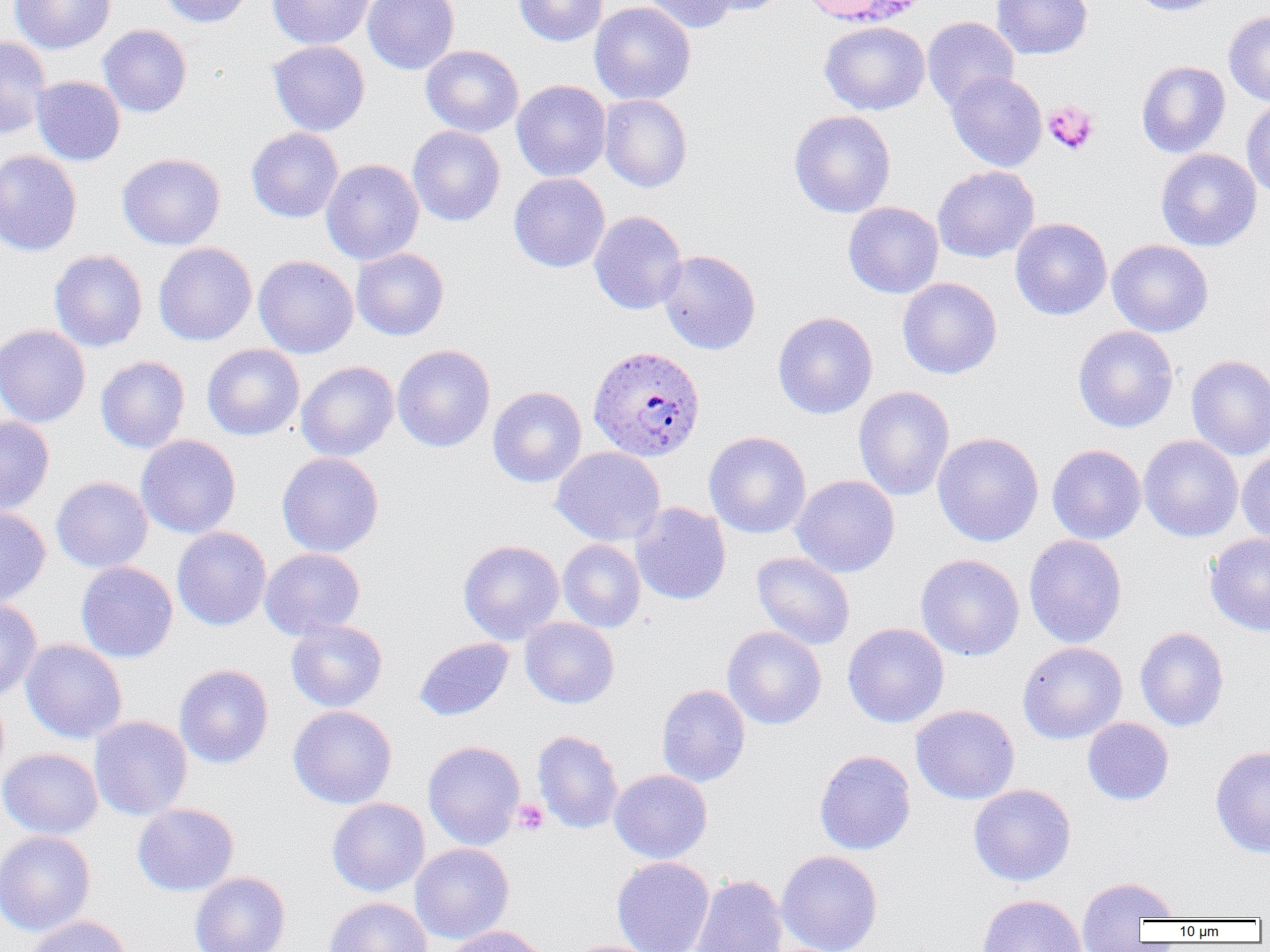
{
  "slide_level_diagnosis": "Plasmodium ovale",
  "image_size": "1270×952 pixels",
  "platelet_locations": "approximate bounding boxes as named x1/y1/x2/y2 corners in pixels: (x1=1042, y1=101, x2=1099, y2=155), (x1=511, y1=799, x2=549, y2=837)",
  "plasmodium_ovale_infected_red_blood_cell_locations": "approximate bounding boxes as named x1/y1/x2/y2 corners in pixels: (x1=588, y1=345, x2=705, y2=462)",
  "uninfected_red_blood_cell_locations": "approximate bounding boxes as named x1/y1/x2/y2 corners in pixels: (x1=10, y1=0, x2=115, y2=54), (x1=159, y1=0, x2=256, y2=27), (x1=266, y1=0, x2=376, y2=49), (x1=362, y1=0, x2=460, y2=75), (x1=513, y1=0, x2=607, y2=46), (x1=639, y1=0, x2=739, y2=33), (x1=696, y1=0, x2=788, y2=16), (x1=991, y1=0, x2=1093, y2=60), (x1=1127, y1=0, x2=1226, y2=16), (x1=589, y1=1, x2=696, y2=105), (x1=954, y1=5, x2=1074, y2=77), (x1=1223, y1=10, x2=1270, y2=106), (x1=922, y1=17, x2=1020, y2=111), (x1=819, y1=20, x2=930, y2=116), (x1=98, y1=24, x2=192, y2=117), (x1=0, y1=36, x2=51, y2=139), (x1=267, y1=40, x2=370, y2=136), (x1=421, y1=45, x2=524, y2=137), (x1=1136, y1=60, x2=1231, y2=158), (x1=946, y1=70, x2=1047, y2=172), (x1=31, y1=76, x2=125, y2=166), (x1=512, y1=80, x2=611, y2=182), (x1=599, y1=94, x2=692, y2=192), (x1=1241, y1=98, x2=1270, y2=201), (x1=789, y1=110, x2=896, y2=218), (x1=407, y1=125, x2=505, y2=226), (x1=246, y1=127, x2=344, y2=223), (x1=1155, y1=148, x2=1262, y2=251), (x1=0, y1=149, x2=83, y2=257), (x1=117, y1=152, x2=225, y2=251), (x1=321, y1=159, x2=424, y2=265), (x1=932, y1=165, x2=1040, y2=263), (x1=508, y1=173, x2=610, y2=272), (x1=843, y1=201, x2=943, y2=298), (x1=589, y1=210, x2=687, y2=314), (x1=1010, y1=218, x2=1112, y2=320), (x1=1107, y1=239, x2=1213, y2=337), (x1=153, y1=242, x2=257, y2=346), (x1=352, y1=247, x2=449, y2=341), (x1=49, y1=250, x2=148, y2=352), (x1=657, y1=250, x2=761, y2=355), (x1=253, y1=255, x2=359, y2=358), (x1=897, y1=277, x2=1002, y2=379), (x1=773, y1=311, x2=878, y2=419), (x1=0, y1=324, x2=90, y2=428), (x1=1073, y1=325, x2=1179, y2=433), (x1=202, y1=343, x2=304, y2=440), (x1=392, y1=344, x2=495, y2=452), (x1=1186, y1=354, x2=1270, y2=460), (x1=95, y1=356, x2=190, y2=454), (x1=296, y1=361, x2=399, y2=461), (x1=488, y1=386, x2=587, y2=487), (x1=853, y1=386, x2=955, y2=501), (x1=0, y1=415, x2=55, y2=516), (x1=703, y1=432, x2=811, y2=538), (x1=932, y1=432, x2=1044, y2=546), (x1=136, y1=434, x2=241, y2=539), (x1=1138, y1=435, x2=1243, y2=542), (x1=1047, y1=444, x2=1147, y2=544), (x1=551, y1=446, x2=665, y2=546), (x1=1236, y1=447, x2=1270, y2=547), (x1=277, y1=452, x2=384, y2=557), (x1=790, y1=475, x2=899, y2=578), (x1=51, y1=476, x2=153, y2=572), (x1=630, y1=502, x2=731, y2=605), (x1=0, y1=506, x2=51, y2=608), (x1=171, y1=527, x2=271, y2=630), (x1=1204, y1=532, x2=1270, y2=637), (x1=1024, y1=534, x2=1127, y2=648), (x1=458, y1=539, x2=564, y2=644), (x1=558, y1=539, x2=646, y2=632), (x1=259, y1=548, x2=365, y2=640), (x1=751, y1=552, x2=855, y2=650), (x1=915, y1=553, x2=1025, y2=661), (x1=75, y1=561, x2=178, y2=663), (x1=0, y1=600, x2=43, y2=702), (x1=520, y1=617, x2=619, y2=709), (x1=286, y1=620, x2=387, y2=712), (x1=843, y1=623, x2=949, y2=728), (x1=722, y1=626, x2=827, y2=730), (x1=1135, y1=627, x2=1229, y2=731), (x1=415, y1=637, x2=513, y2=721), (x1=20, y1=639, x2=127, y2=744), (x1=1017, y1=641, x2=1127, y2=744), (x1=174, y1=664, x2=274, y2=768), (x1=656, y1=684, x2=751, y2=787), (x1=910, y1=704, x2=1020, y2=805), (x1=288, y1=705, x2=397, y2=809), (x1=89, y1=716, x2=192, y2=820), (x1=1082, y1=717, x2=1173, y2=806), (x1=532, y1=730, x2=624, y2=833), (x1=423, y1=740, x2=525, y2=850), (x1=1210, y1=745, x2=1270, y2=858), (x1=0, y1=748, x2=103, y2=839), (x1=814, y1=750, x2=916, y2=855), (x1=609, y1=769, x2=712, y2=864), (x1=968, y1=784, x2=1076, y2=886), (x1=327, y1=797, x2=430, y2=896), (x1=132, y1=803, x2=239, y2=896), (x1=0, y1=830, x2=96, y2=937), (x1=409, y1=843, x2=514, y2=944), (x1=775, y1=850, x2=883, y2=952), (x1=612, y1=857, x2=715, y2=952), (x1=189, y1=872, x2=290, y2=952), (x1=689, y1=874, x2=788, y2=952), (x1=1075, y1=876, x2=1180, y2=947), (x1=975, y1=893, x2=1088, y2=952), (x1=324, y1=897, x2=433, y2=952), (x1=26, y1=915, x2=134, y2=952), (x1=442, y1=924, x2=554, y2=952), (x1=562, y1=939, x2=664, y2=952)",
  "field_of_view": "single",
  "modality": "light microscopy",
  "magnification": "1000x",
  "preparation": "thin blood smear"
}